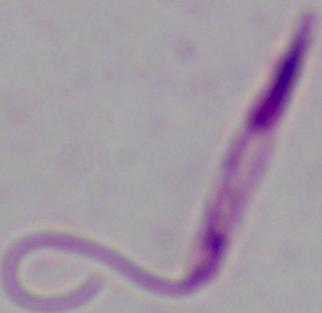

identification = Leishmania
modality = micrograph
magnification = 1000x